Classify this cell by malaria status.
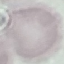

It is uninfected.

Acquired by smartphone through the microscope eyepiece. Giemsa-stained preparation. Automatically extracted cell patch, resized to 64 × 64 pixels. Thin blood film.